Locate every uninfected red blood cell.
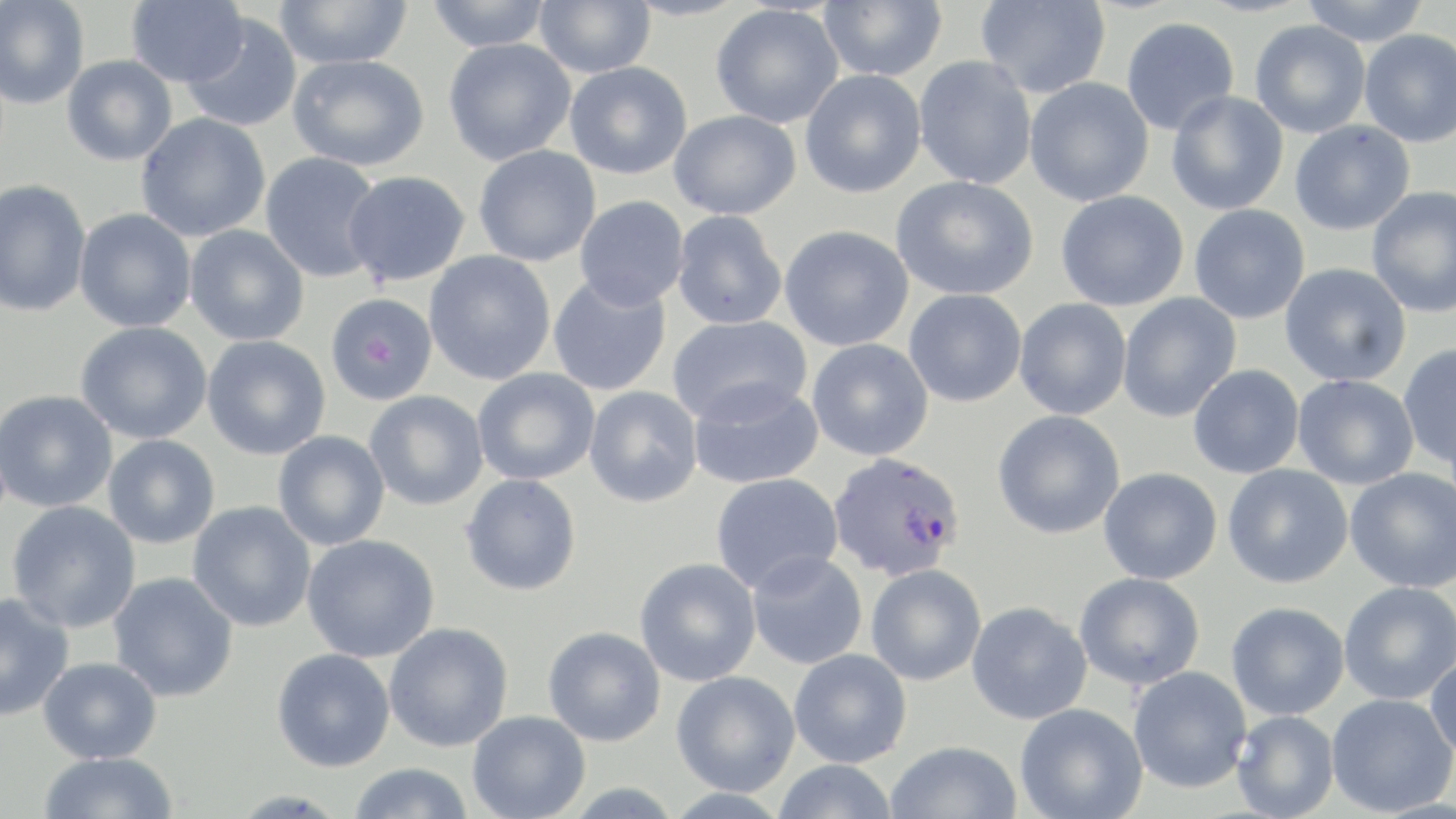

Approximate bounding boxes as (x1,y1)-(x2,y2) corner pairs in pixels.
Uninfected red blood cells: (0,0)-(90,109), (126,0)-(248,88), (274,0)-(413,69), (424,0)-(554,52), (534,0)-(656,77), (621,0)-(750,21), (975,0)-(1111,100), (1299,0)-(1431,46), (819,1)-(947,81), (710,5)-(844,129), (181,12)-(302,133), (1121,16)-(1239,136), (1250,20)-(1370,138), (1359,29)-(1456,147), (443,38)-(576,165), (288,54)-(429,171), (62,55)-(177,166), (914,57)-(1037,190), (564,61)-(692,179), (799,70)-(927,199), (1024,77)-(1154,207), (1165,91)-(1289,216), (669,110)-(801,220), (136,113)-(271,242), (1289,120)-(1415,236), (473,145)-(601,267), (260,151)-(383,282), (342,170)-(471,286), (890,176)-(1039,301), (0,179)-(91,317), (1366,186)-(1456,318), (1054,191)-(1189,312), (575,196)-(689,309), (1188,204)-(1310,324), (74,208)-(197,333), (671,211)-(787,330), (185,225)-(309,346), (779,225)-(913,351), (424,251)-(556,385), (1279,263)-(1412,388), (547,274)-(672,397), (903,289)-(1026,407), (325,292)-(438,406), (1116,293)-(1241,423), (1013,298)-(1131,420), (667,314)-(813,425), (75,321)-(212,444), (202,335)-(331,460), (806,339)-(933,461), (1397,344)-(1456,470), (1188,365)-(1304,479), (472,368)-(600,486), (1292,375)-(1418,490), (688,378)-(824,489), (584,386)-(703,508), (0,390)-(117,513), (364,390)-(489,511), (992,410)-(1125,539), (272,431)-(390,551), (103,434)-(220,548), (1222,464)-(1353,589), (1098,467)-(1222,585), (1344,468)-(1456,593), (460,473)-(582,596), (710,473)-(843,594), (5,501)-(141,633), (187,501)-(316,633), (302,534)-(440,663), (746,551)-(867,669), (634,558)-(761,687), (865,564)-(986,686), (108,572)-(239,702), (1073,572)-(1205,689), (1338,581)-(1456,705), (0,593)-(74,722), (966,601)-(1092,725), (1226,601)-(1349,720), (384,623)-(513,752), (543,626)-(666,747), (271,648)-(395,772), (788,649)-(911,768), (1425,653)-(1456,761), (38,657)-(161,763), (1128,667)-(1251,794), (671,671)-(800,796), (1326,692)-(1455,817), (1015,703)-(1148,819), (1232,710)-(1340,819), (467,711)-(590,818), (885,741)-(1021,819), (38,752)-(179,819), (772,759)-(899,819), (347,763)-(474,819).

Summary:
  - Plasmodium falciparum-infected red blood cell locations: (828,452)-(966,581)
  - Slide-level diagnosis: Plasmodium falciparum
  - Magnification: 1000x
  - Image size: 1456×819 pixels
  - Stain: May-Grünwald-Giemsa
  - Preparation: thin blood smear
  - Field of view: single
  - Modality: optical microscopy